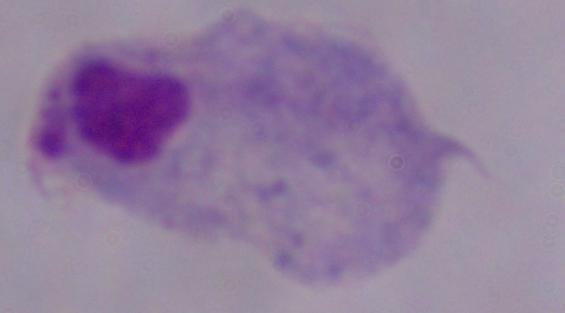

Photomicrograph. A trichomonad is shown. Captured at 1000x magnification.